Assess the morphology of the red blood cells.
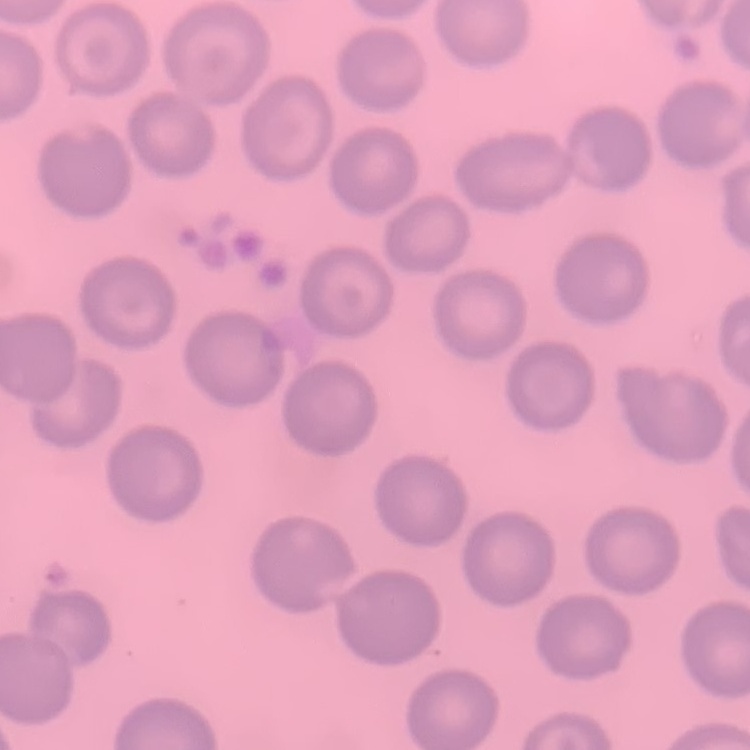
They show no rouleaux formation.

Summary:
  - Stain: Field's or Giemsa
  - Image type: square crop of a larger photomicrograph
  - Preparation: thin blood film